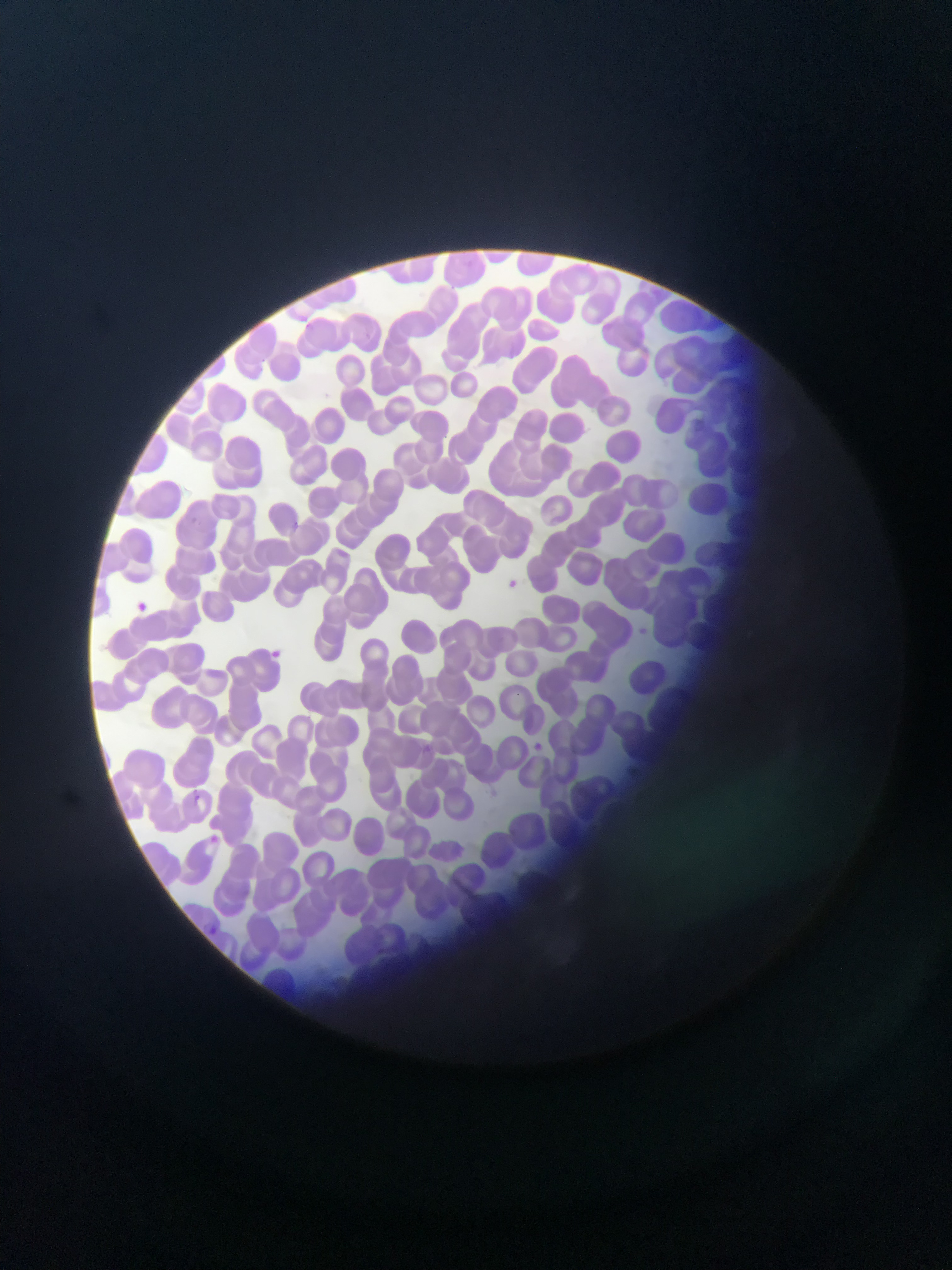 Approximate bounding boxes as left top right bottom in pixels. Plasmodium parasite locations: 506 578 523 594; 128 597 153 618; 634 626 652 644; 527 739 548 757; 624 759 644 787; 204 922 221 938. Thin blood film. Collected in Ghana. Photographed through a microscope with a mobile-phone camera. Single field of view. Image is 952×1270 pixels.